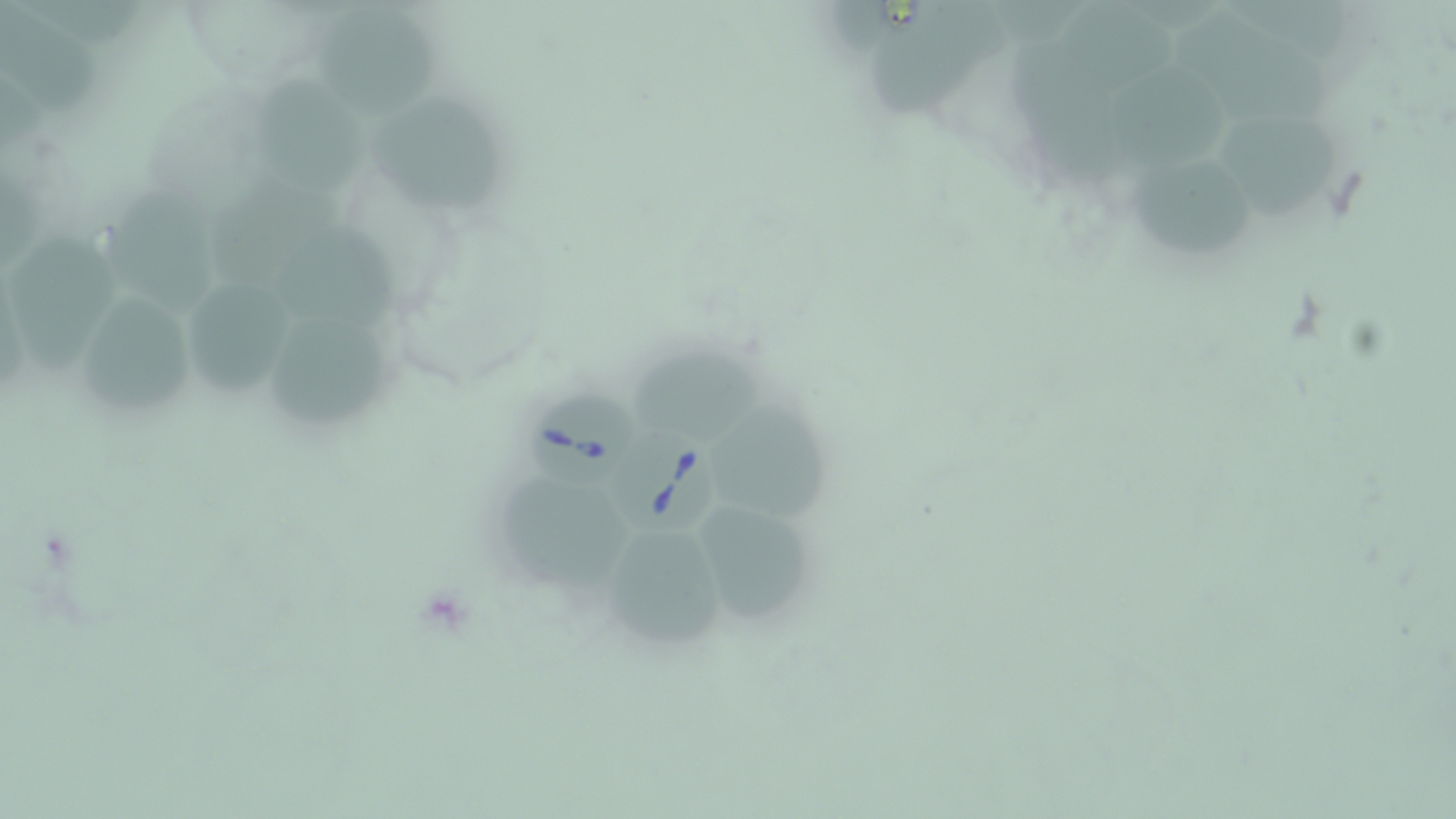
slide-level diagnosis = Babesia divergens
magnification = 1000x
preparation = thin blood film
field of view = one of a larger specimen
Babesia divergens-infected red blood cell locations = approximate bounding boxes as (x1, y1, x2, y2) in pixels: (527, 389, 636, 486), (612, 423, 730, 533)
uninfected red blood cell locations = approximate bounding boxes as (x1, y1, x2, y2) in pixels: (3, 3, 100, 115), (317, 6, 445, 121), (872, 10, 986, 114), (1169, 10, 1340, 131), (1106, 66, 1235, 176), (257, 78, 361, 197), (373, 97, 507, 214), (1215, 112, 1344, 220), (1136, 150, 1256, 263), (204, 175, 346, 288), (108, 185, 218, 318), (279, 223, 401, 332), (12, 231, 121, 373), (186, 283, 288, 394), (80, 296, 191, 409), (270, 314, 386, 427), (628, 347, 764, 444), (717, 399, 832, 526), (500, 478, 632, 593), (707, 509, 810, 622), (594, 521, 731, 652)
modality = optical microscopy
stain = May-Grünwald-Giemsa
image size = 1456×819 pixels